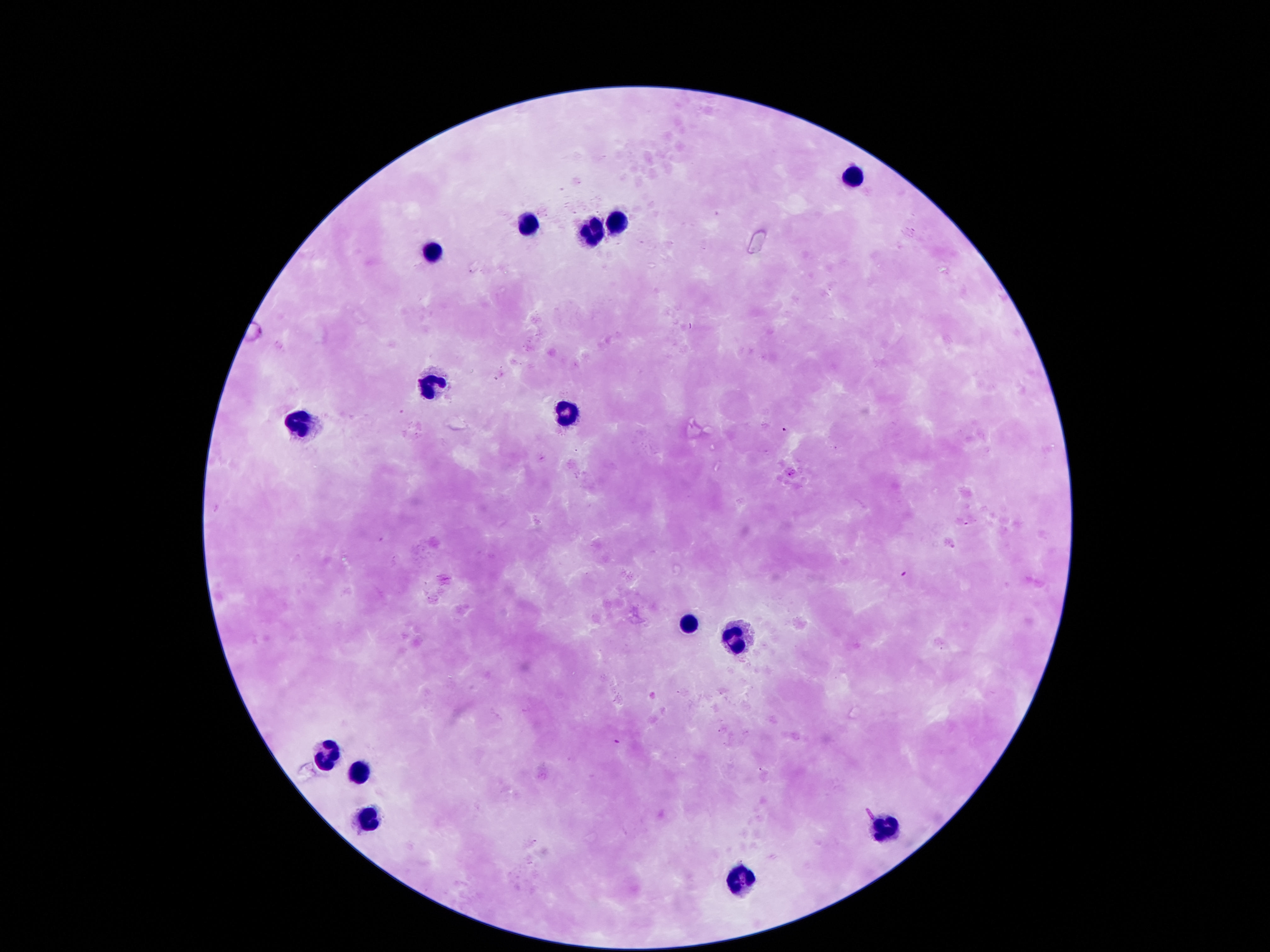

magnification = 100x
capture = smartphone camera through the microscope eyepiece
leukocyte locations = approximate centers as {x, y} in pixels: {849, 172}, {529, 219}, {616, 219}, {593, 228}, {432, 251}, {425, 385}, {564, 408}, {296, 424}, {687, 622}, {732, 635}, {322, 754}, {358, 771}, {367, 816}, {884, 824}, {742, 877}
preparation = thick blood film
patient malaria status = uninfected
image size = 1270×952 pixels
stain = Giemsa
field of view = single